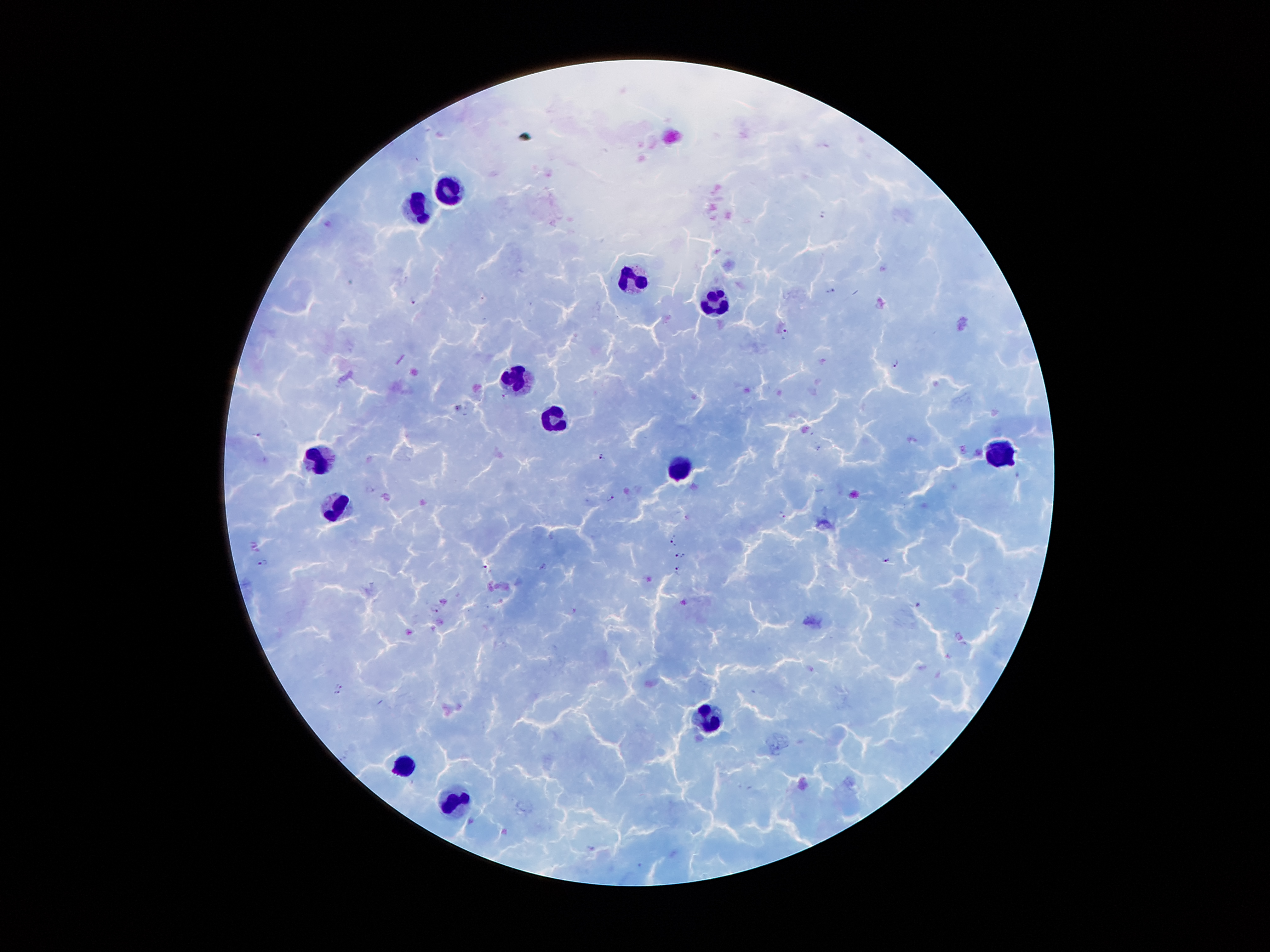 Approximate centers as {x, y} in pixels. Plasmodium parasite locations: {824, 214}, {831, 291}, {413, 301}, {786, 331}, {895, 364}, {503, 396}, {458, 408}, {257, 434}, {819, 448}, {600, 456}, {1018, 474}, {610, 498}, {782, 515}, {673, 541}, {680, 555}, {885, 559}, {263, 562}, {484, 567}, {677, 569}, {917, 605}, {435, 610}, {574, 610}, {339, 685}, {337, 694}, {342, 758}, {591, 848}. Leukocyte locations: {452, 191}, {419, 205}, {636, 281}, {713, 305}, {518, 378}, {554, 416}, {1004, 454}, {318, 460}, {687, 472}, {339, 508}, {709, 721}, {402, 765}, {456, 803}. Smartphone photograph taken through the microscope eyepiece. Patient malaria status: positive for Plasmodium falciparum. Image is 1270×952 pixels. Single field of view. Giemsa-stained preparation. Thick blood film. 100x magnification.